Locate and identify every blood parasite.
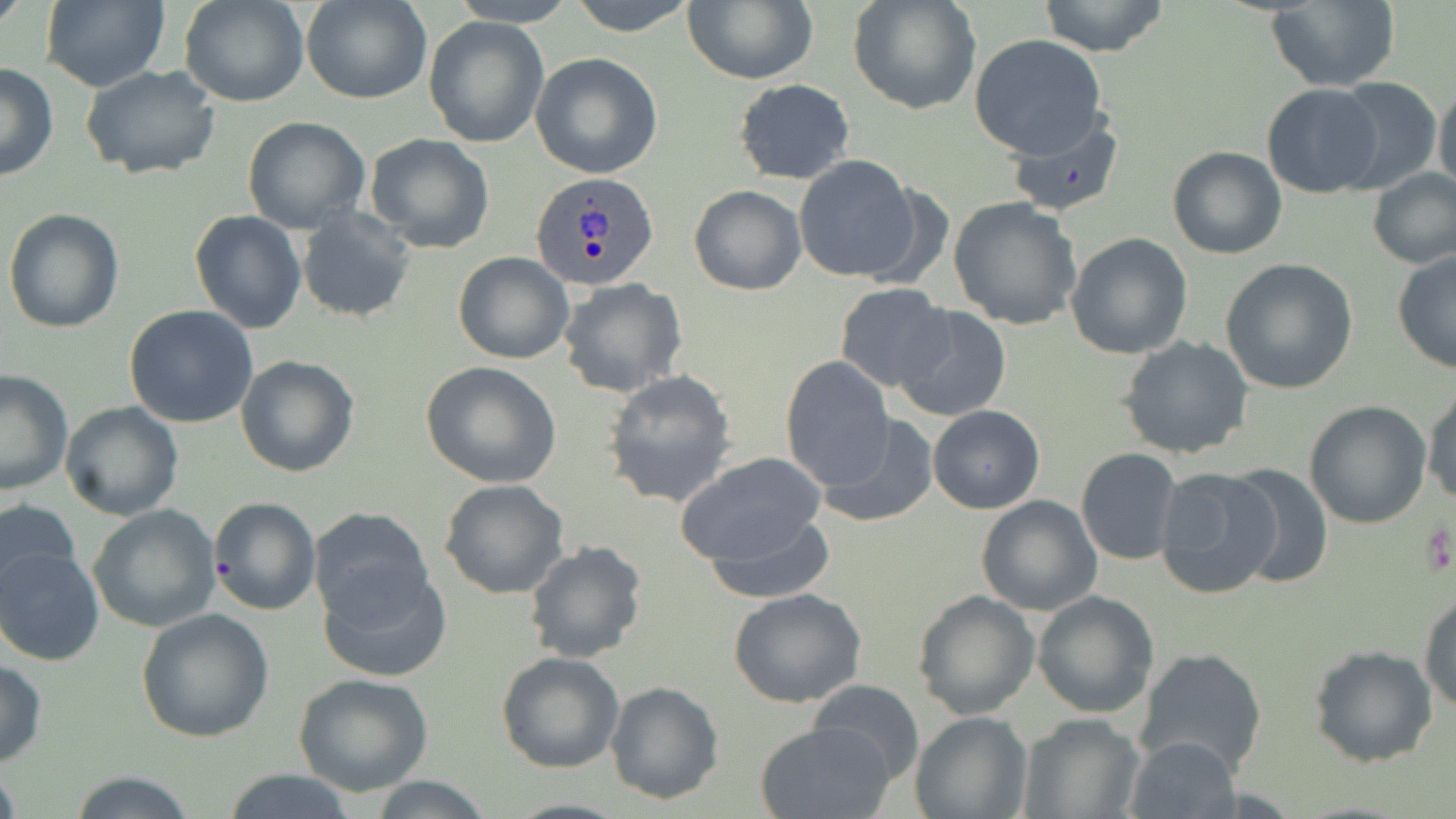
Approximate bounding boxes as (x1,y1)-(x2,y2) corner pairs in pixels.
Plasmodium ovale-infected red blood cells: (530,170)-(657,290).
No Plasmodium falciparum, Plasmodium malariae, Plasmodium vivax, Babesia divergens, or Trypanosoma brucei observed.

slide_level_diagnosis: Plasmodium ovale
modality: optical microscopy
uninfected_red_blood_cell_locations: 'approximate bounding boxes as (x1,y1)-(x2,y2) corner pairs in pixels: (39,0)-(168,93), (179,0)-(310,106), (303,0)-(432,105), (450,0)-(577,27), (567,0)-(698,37), (849,0)-(983,114), (1037,0)-(1169,58), (682,1)-(818,85), (1265,2)-(1399,90), (424,17)-(548,148), (970,34)-(1107,158), (530,52)-(663,178), (0,64)-(58,181), (82,66)-(224,181), (1329,77)-(1443,193), (734,78)-(855,185), (1434,79)-(1456,197), (1261,84)-(1384,197), (241,115)-(370,234), (1008,115)-(1123,218), (363,132)-(496,254), (1167,145)-(1287,259), (794,155)-(924,283), (1366,167)-(1456,270), (689,185)-(806,295), (947,196)-(1083,332), (297,205)-(417,325), (3,208)-(125,334), (189,210)-(306,333), (1065,232)-(1193,359), (1392,250)-(1456,375), (453,251)-(574,364), (1220,258)-(1358,394), (558,277)-(688,398), (834,283)-(955,392), (122,304)-(259,428), (891,304)-(1013,423), (1118,336)-(1256,459), (235,355)-(360,478), (780,357)-(896,488), (420,362)-(560,488), (0,368)-(76,497), (601,369)-(737,509), (1424,383)-(1456,510), (1303,400)-(1432,529), (59,401)-(184,520), (928,405)-(1044,514), (815,413)-(938,528), (1076,447)-(1184,565), (676,451)-(830,571), (1223,462)-(1334,589), (1155,465)-(1282,597), (439,480)-(570,600), (975,495)-(1102,615), (207,496)-(322,617), (0,497)-(82,603), (87,504)-(220,631), (308,506)-(436,628), (700,509)-(837,603), (522,540)-(648,665), (0,545)-(105,666), (320,564)-(452,683), (728,588)-(868,708), (1420,588)-(1456,713), (912,590)-(1040,720), (1033,590)-(1160,718), (136,607)-(275,742), (1307,644)-(1439,768), (1134,647)-(1270,778), (496,651)-(623,773), (0,659)-(47,766), (292,672)-(433,796), (807,678)-(925,783), (605,681)-(724,805), (910,711)-(1033,819), (1018,712)-(1144,818), (754,720)-(898,819), (1124,736)-(1242,819), (215,770)-(365,818), (67,772)-(198,818), (361,775)-(496,818)'
magnification: 1000x
stain: May-Grünwald-Giemsa
image_size: 1456×819 pixels
preparation: thin blood film
platelet_locations: 'approximate bounding boxes as (x1,y1)-(x2,y2) corner pairs in pixels: (1422,517)-(1454,582)'
field_of_view: single